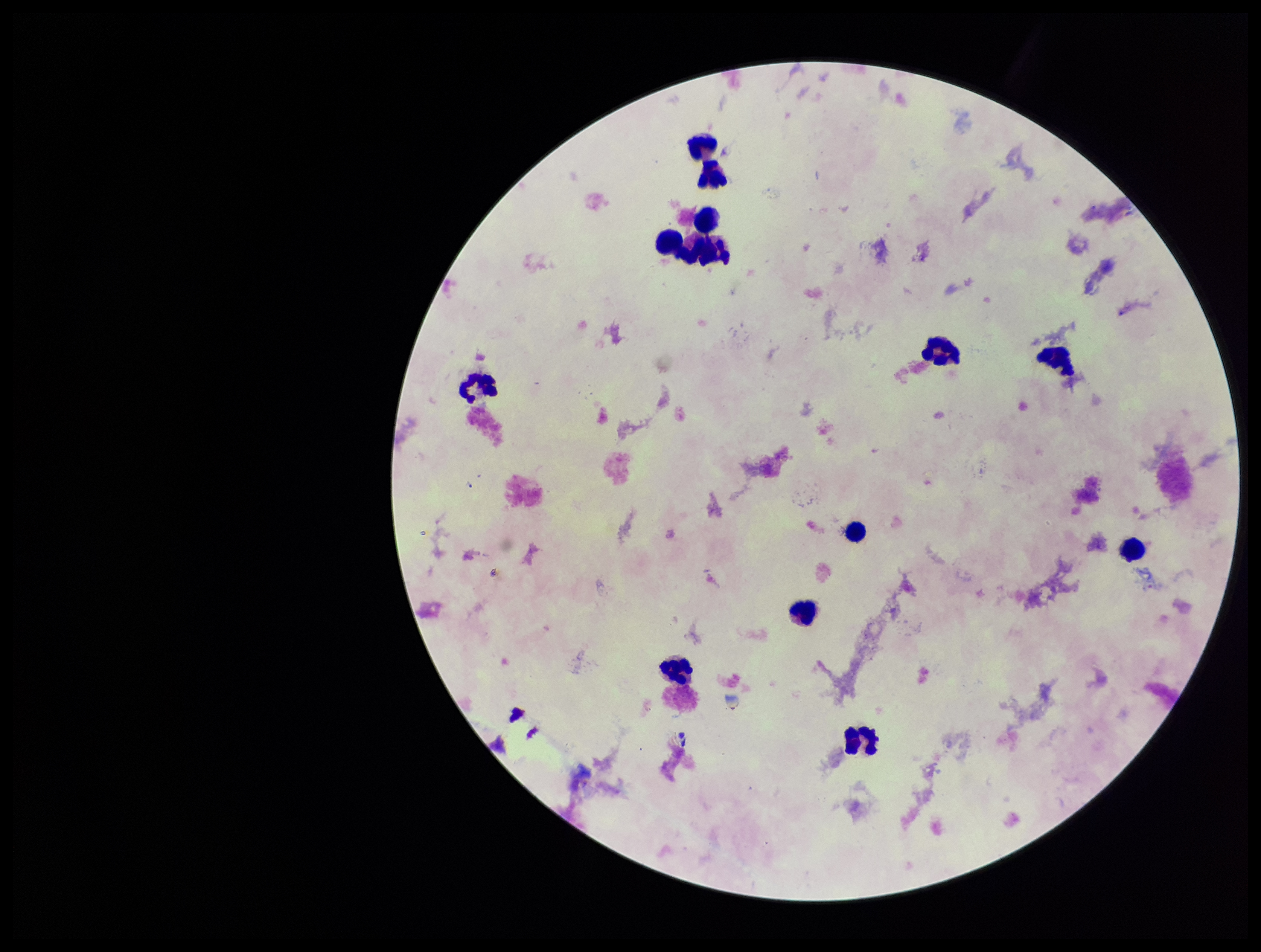 Preparation: thick. Patient malaria status: negative. Plasmodium parasites: none seen. Photographed through the microscope eyepiece with a smartphone camera. Parasite count: 0. Stained with Giemsa. One field from this slide. Image is 1261×952 pixels. Leukocyte count: 12.